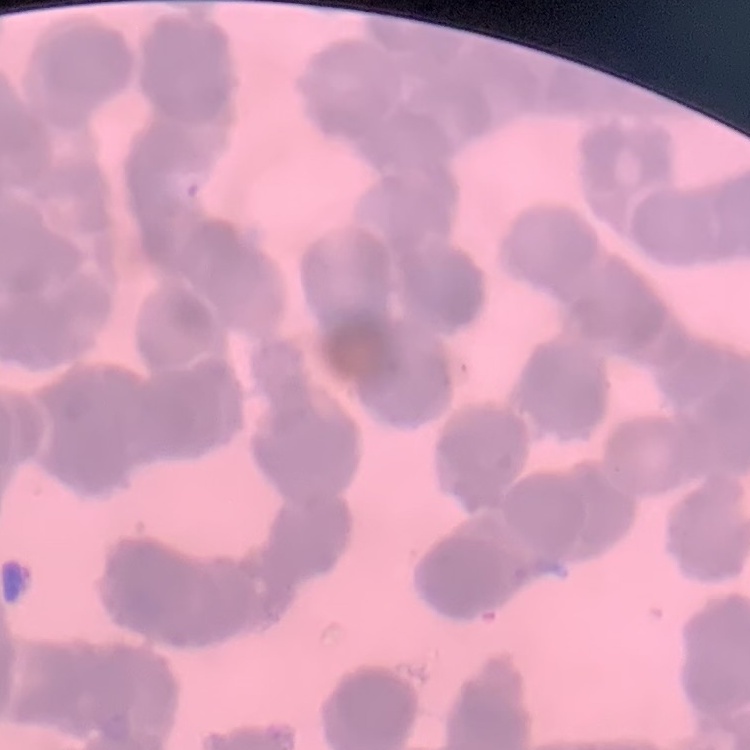 The erythrocytes show rouleaux formation. One tile cut from a larger photomicrograph. Stained with either Field's or Giemsa. Thin blood film.